Name the parasite shown.
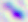

Toxoplasma gondii.

magnification: 400x
modality: photomicrograph